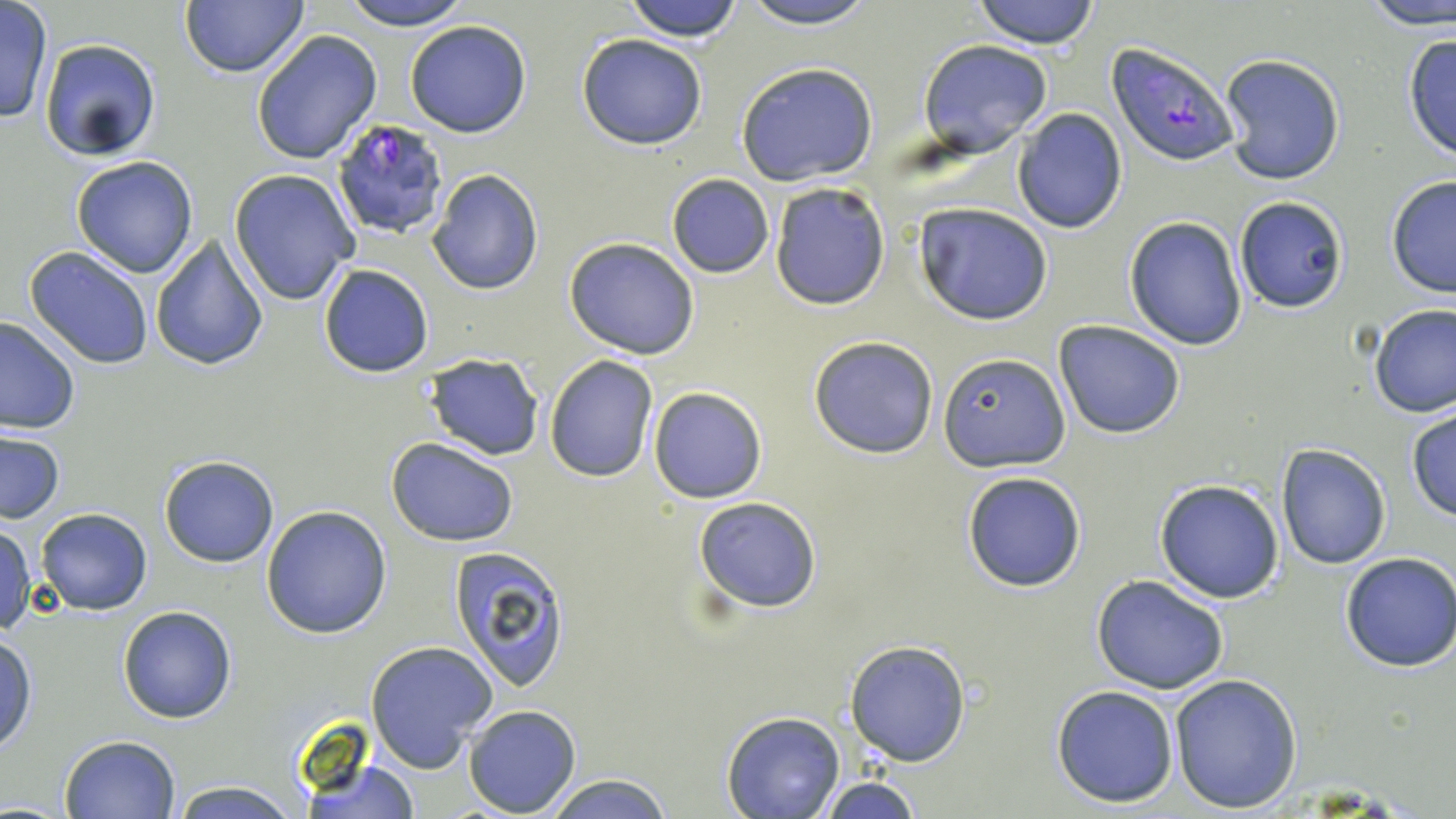
Approximate bounding boxes as named x1/y1/x2/y2 corners in pixels. Uninfected red blood cell locations: (x1=178, y1=0, x2=311, y2=79), (x1=338, y1=0, x2=476, y2=30), (x1=621, y1=0, x2=746, y2=42), (x1=736, y1=0, x2=883, y2=29), (x1=973, y1=0, x2=1101, y2=48), (x1=1356, y1=0, x2=1455, y2=30), (x1=0, y1=3, x2=53, y2=124), (x1=405, y1=19, x2=531, y2=137), (x1=252, y1=30, x2=381, y2=164), (x1=1402, y1=33, x2=1456, y2=162), (x1=576, y1=34, x2=708, y2=149), (x1=39, y1=38, x2=162, y2=162), (x1=918, y1=39, x2=1054, y2=156), (x1=1219, y1=53, x2=1346, y2=186), (x1=736, y1=62, x2=878, y2=187), (x1=1010, y1=109, x2=1127, y2=232), (x1=70, y1=155, x2=199, y2=279), (x1=229, y1=168, x2=359, y2=305), (x1=426, y1=169, x2=545, y2=296), (x1=666, y1=173, x2=774, y2=278), (x1=1385, y1=175, x2=1456, y2=299), (x1=769, y1=181, x2=892, y2=309), (x1=1235, y1=197, x2=1349, y2=313), (x1=912, y1=202, x2=1053, y2=325), (x1=1124, y1=216, x2=1249, y2=351), (x1=150, y1=234, x2=270, y2=372), (x1=564, y1=237, x2=700, y2=359), (x1=23, y1=246, x2=154, y2=369), (x1=317, y1=264, x2=434, y2=378), (x1=1368, y1=303, x2=1455, y2=418), (x1=0, y1=315, x2=80, y2=434), (x1=1053, y1=320, x2=1187, y2=439), (x1=809, y1=335, x2=939, y2=458), (x1=938, y1=351, x2=1068, y2=470), (x1=423, y1=354, x2=545, y2=459), (x1=544, y1=354, x2=661, y2=482), (x1=648, y1=387, x2=766, y2=502), (x1=1406, y1=405, x2=1456, y2=523), (x1=0, y1=430, x2=66, y2=523), (x1=387, y1=437, x2=519, y2=547), (x1=1276, y1=443, x2=1392, y2=570), (x1=158, y1=456, x2=280, y2=568), (x1=960, y1=469, x2=1089, y2=593), (x1=1154, y1=478, x2=1285, y2=604), (x1=693, y1=496, x2=822, y2=613), (x1=260, y1=505, x2=393, y2=639), (x1=36, y1=508, x2=152, y2=614), (x1=0, y1=523, x2=36, y2=635), (x1=447, y1=544, x2=572, y2=692), (x1=1340, y1=551, x2=1456, y2=672), (x1=1091, y1=574, x2=1230, y2=695), (x1=117, y1=605, x2=237, y2=724), (x1=1, y1=633, x2=37, y2=755), (x1=364, y1=639, x2=498, y2=773), (x1=845, y1=640, x2=971, y2=768), (x1=1169, y1=674, x2=1302, y2=813), (x1=1050, y1=685, x2=1181, y2=808), (x1=462, y1=704, x2=581, y2=817), (x1=722, y1=712, x2=843, y2=819), (x1=59, y1=735, x2=182, y2=819), (x1=298, y1=756, x2=421, y2=818), (x1=539, y1=771, x2=675, y2=818), (x1=813, y1=776, x2=924, y2=818), (x1=168, y1=780, x2=305, y2=819). Plasmodium falciparum-infected red blood cell locations: (x1=1108, y1=41, x2=1238, y2=166), (x1=329, y1=117, x2=455, y2=240). Slide-level diagnosis: Plasmodium falciparum. Thin blood film. May-Grünwald-Giemsa-stained preparation. 1000x magnification. Image is 1456×819 pixels. Single field of view. Light microscopy.